Give the position of every leukocyte visible.
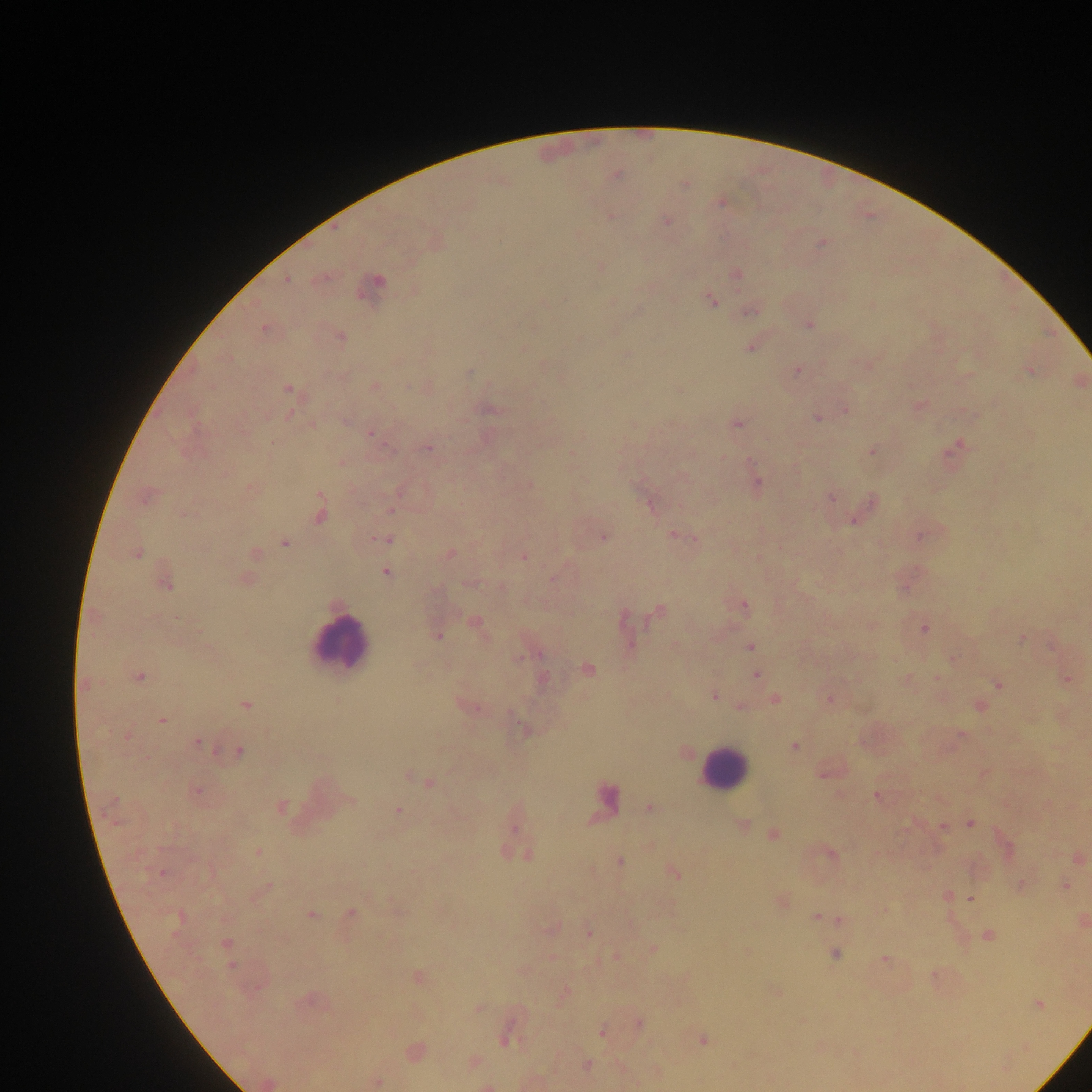
Approximate centers as [x, y] in pixels.
Leukocytes: [340, 642], [723, 769], [605, 800].

{
  "preparation": "thick blood film",
  "field_of_view": "single",
  "malaria_parasite_locations": "approximate centers as [x, y] in pixels: [616, 174], [684, 183], [720, 201], [611, 215], [665, 220], [434, 242], [822, 243], [600, 267], [735, 274], [287, 279], [373, 284], [710, 301], [751, 310], [808, 324], [264, 328], [340, 336], [579, 338], [750, 346], [866, 364], [797, 370], [1029, 370], [374, 385], [288, 389], [919, 405], [845, 409], [489, 410], [817, 417], [735, 423], [370, 433], [957, 445], [427, 448], [871, 451], [341, 462], [529, 484], [757, 485], [251, 488], [146, 495], [831, 497], [650, 504], [868, 504], [391, 508], [320, 513], [184, 514], [858, 514], [674, 535], [919, 535], [602, 536], [686, 537], [386, 538], [694, 538], [284, 542], [136, 553], [254, 554], [448, 554], [523, 555], [386, 572], [244, 578], [554, 578], [164, 580], [471, 583], [743, 605], [658, 611], [475, 623], [624, 623], [871, 624], [924, 628], [437, 635], [1021, 637], [673, 645], [1053, 645], [749, 646], [952, 659], [586, 669], [756, 674], [139, 676], [541, 678], [938, 678], [1067, 678], [907, 680], [997, 684], [85, 685], [713, 695], [774, 698], [829, 698], [245, 704], [978, 705], [468, 706], [740, 706], [161, 720], [526, 731], [960, 734], [126, 737], [197, 742], [793, 746], [239, 751], [683, 753], [825, 771], [983, 772], [406, 774], [429, 782], [196, 791], [876, 795], [939, 798], [351, 800], [281, 807], [650, 807], [398, 810], [741, 823], [970, 823], [943, 826], [774, 835], [257, 852], [829, 853], [526, 854], [1077, 856], [619, 861], [161, 873], [674, 873], [1020, 885], [1064, 886], [266, 887], [946, 897], [970, 898], [781, 901], [883, 911], [350, 914], [310, 915], [816, 917], [179, 918], [839, 919], [1081, 921], [551, 929], [588, 932], [986, 935], [226, 943], [652, 949], [835, 953], [615, 957], [884, 959], [935, 976], [417, 978], [775, 991], [565, 993], [309, 1002], [1037, 1005], [478, 1007], [801, 1021], [638, 1024], [602, 1031], [508, 1033], [702, 1040], [414, 1052], [472, 1061], [587, 1065], [375, 1081], [531, 1081], [267, 1082], [489, 1085]",
  "capture": "mobile-phone photograph through a microscope",
  "image_size": "1092×1092 pixels",
  "country": "Ghana"
}